Report the malaria status of this cell.
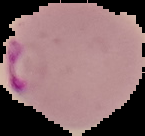
Parasitized.

Segmented cell region on a black background. Image is 145×136 pixels. From a thin blood film.